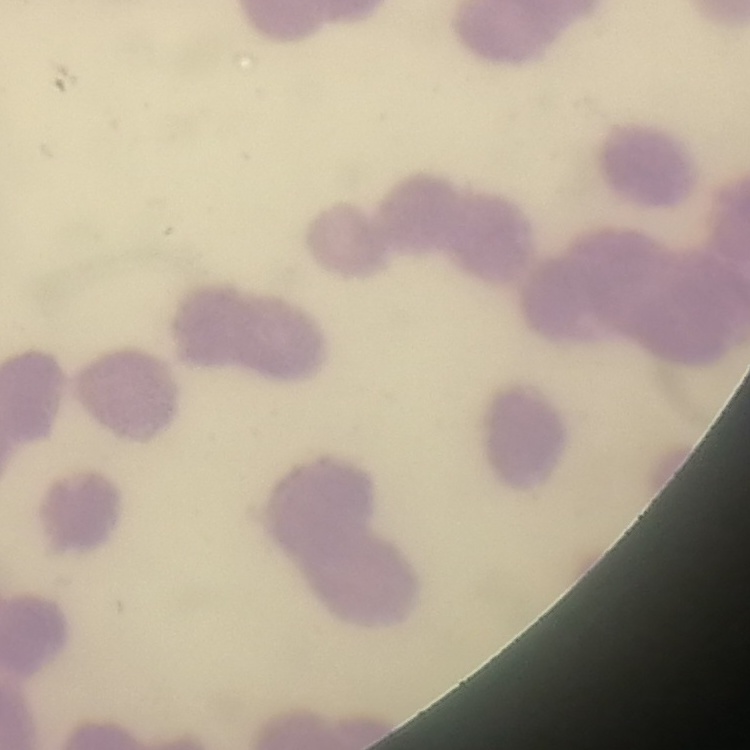
red_blood_cell_morphology: rouleaux formation
preparation: thin peripheral smear
image_type: one tile cut from a larger photomicrograph
stain: Field's or Giemsa